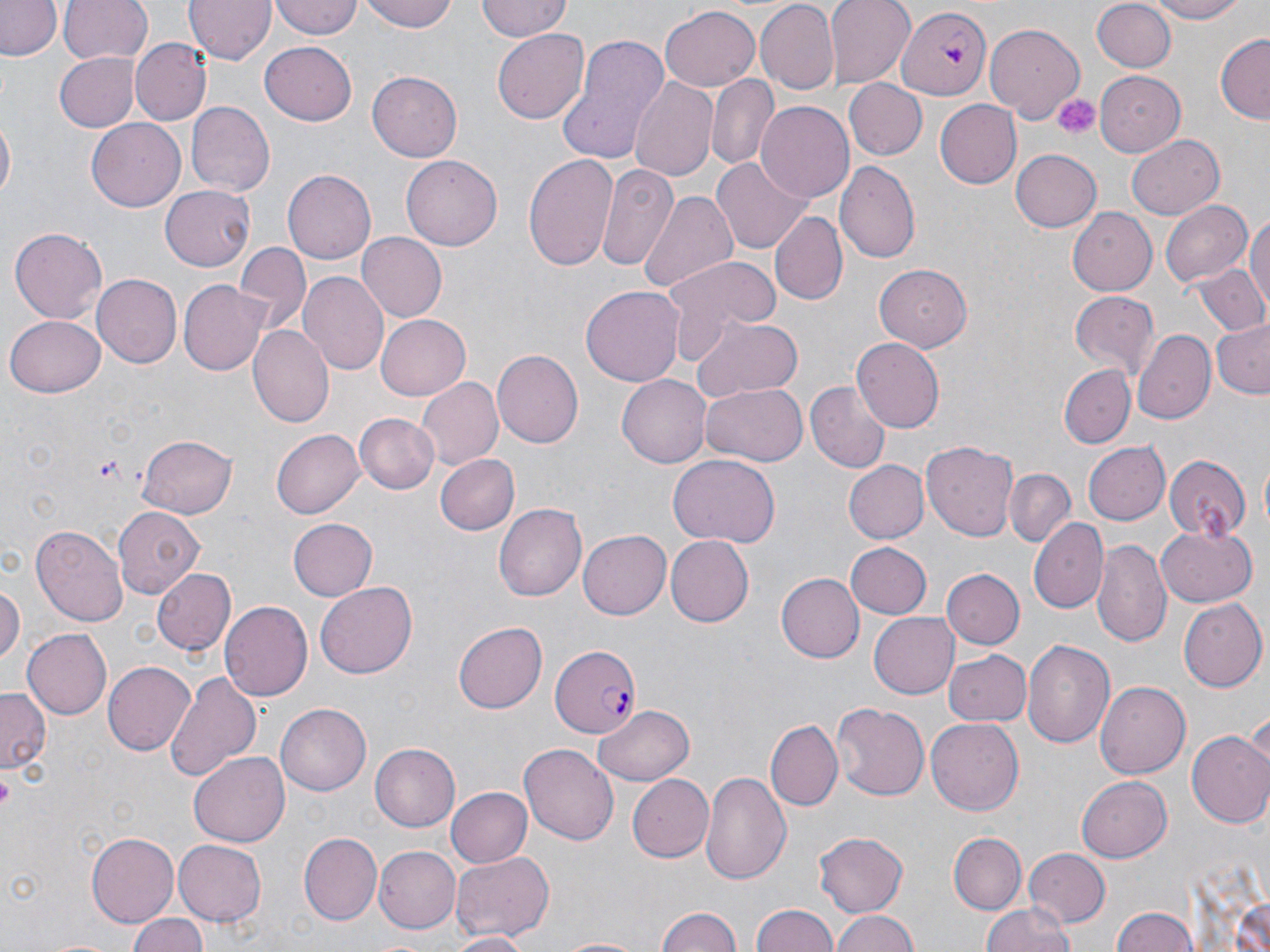
slide-level diagnosis = Plasmodium falciparum
stain = May-Grünwald-Giemsa
Plasmodium falciparum-infected red blood cell locations = approximate bounding boxes as (x1,y1)-(x2,y2) corner pairs in pixels: (897,6)-(990,99), (550,644)-(643,738)
field of view = one of a larger specimen
platelet locations = approximate bounding boxes as (x1,y1)-(x2,y2) corner pairs in pixels: (1048,90)-(1103,141), (91,454)-(123,481), (0,776)-(13,809)
image size = 1270×952 pixels
magnification = 1000x
modality = optical microscopy
uninfected red blood cell locations = approximate bounding boxes as (x1,y1)-(x2,y2) corner pairs in pixels: (2,0)-(60,61), (59,0)-(153,66), (185,0)-(275,64), (269,0)-(362,40), (360,0)-(457,32), (476,0)-(572,43), (823,0)-(915,87), (1145,0)-(1253,24), (1092,1)-(1177,73), (757,2)-(839,93), (660,3)-(760,91), (985,23)-(1086,119), (554,27)-(673,167), (493,31)-(589,121), (1215,32)-(1269,123), (130,38)-(210,124), (259,43)-(357,125), (55,52)-(140,132), (1094,70)-(1186,157), (366,72)-(462,163), (708,75)-(779,170), (628,76)-(720,182), (844,78)-(926,161), (932,99)-(1021,188), (187,102)-(274,195), (755,102)-(855,205), (1,117)-(16,201), (87,120)-(185,210), (1125,134)-(1225,219), (1009,148)-(1101,233), (522,153)-(620,269), (402,155)-(500,251), (709,156)-(815,253), (836,159)-(921,264), (598,163)-(679,271), (281,169)-(374,266), (638,186)-(739,295), (161,187)-(255,270), (1161,199)-(1251,289), (1067,207)-(1157,295), (1245,210)-(1270,324), (771,212)-(846,305), (8,227)-(107,325), (358,233)-(446,324), (236,242)-(308,331), (665,255)-(779,345), (873,264)-(973,352), (1196,264)-(1269,337), (298,272)-(388,375), (92,274)-(181,369), (179,279)-(271,376), (580,286)-(686,386), (1067,290)-(1159,378), (7,315)-(106,395), (375,315)-(469,400), (691,317)-(804,402), (1209,318)-(1270,399), (249,325)-(334,430), (1132,328)-(1216,425), (852,336)-(945,430), (492,350)-(583,449), (1062,364)-(1135,448), (618,373)-(713,466), (416,377)-(504,470), (806,380)-(891,474), (700,385)-(807,467), (356,413)-(439,494), (271,429)-(365,520), (137,434)-(238,520), (1084,440)-(1170,526), (921,441)-(1020,540), (1164,452)-(1251,542), (436,455)-(519,534), (667,456)-(779,547), (841,460)-(927,544), (1005,467)-(1075,545), (495,502)-(587,601), (113,508)-(203,598), (1029,516)-(1108,612), (287,517)-(375,602), (31,526)-(128,626), (1156,526)-(1255,608), (579,530)-(671,619), (664,534)-(752,626), (1092,537)-(1173,647), (843,543)-(931,618), (940,568)-(1022,650), (156,570)-(236,655), (775,573)-(862,663), (315,582)-(418,679), (0,583)-(23,667), (1180,599)-(1267,691), (219,602)-(311,700), (868,610)-(959,697), (453,621)-(547,713), (22,629)-(112,720), (1022,638)-(1115,752), (942,648)-(1032,726), (103,661)-(197,756), (164,669)-(262,782), (1095,681)-(1192,778), (0,687)-(49,774), (830,701)-(929,802), (593,702)-(694,784), (277,703)-(370,795), (926,718)-(1024,815), (767,721)-(841,810), (1186,729)-(1270,827), (520,742)-(618,843), (370,743)-(460,832), (190,751)-(292,846), (701,769)-(791,884), (628,774)-(713,863), (1076,775)-(1172,863), (447,789)-(531,867), (300,831)-(380,923), (813,832)-(909,916), (949,832)-(1025,914), (85,833)-(179,928), (172,839)-(267,926), (374,846)-(460,933), (1023,847)-(1111,926), (450,851)-(554,942), (750,902)-(841,952), (979,904)-(1078,952), (653,905)-(745,952), (1109,908)-(1199,952), (829,910)-(919,952), (126,912)-(209,952), (443,933)-(531,952), (554,935)-(647,952)
preparation = thin blood smear